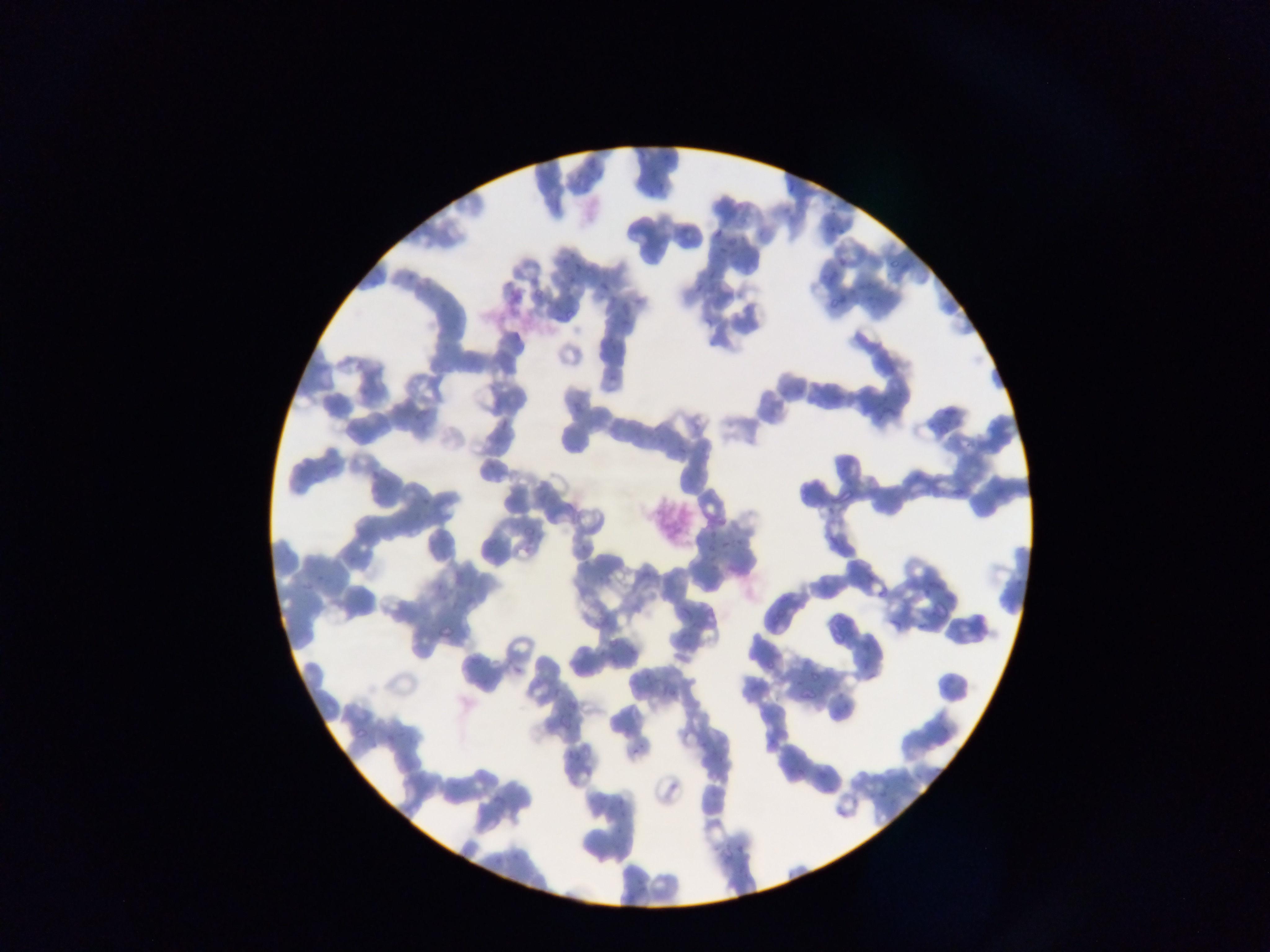

Approximate bounding boxes as (left, top, right, bottom) in pixels. Malaria parasite locations (subset; some below the resolvable size): (780, 177, 796, 195), (645, 179, 671, 194), (775, 198, 797, 224), (831, 220, 845, 233), (676, 222, 689, 236), (712, 222, 726, 236), (715, 244, 729, 258), (556, 249, 578, 267), (880, 259, 896, 277), (572, 261, 591, 274), (821, 267, 839, 287), (690, 277, 706, 299), (599, 278, 611, 290), (859, 280, 877, 303), (827, 288, 845, 310), (550, 291, 568, 313), (618, 296, 629, 317), (829, 382, 848, 401), (873, 397, 899, 422), (936, 404, 962, 424), (494, 417, 513, 437), (363, 470, 381, 488), (950, 477, 969, 496), (833, 485, 854, 504), (413, 498, 430, 509), (705, 518, 720, 548), (724, 525, 750, 550), (509, 542, 542, 559), (297, 580, 317, 596), (440, 620, 455, 642), (510, 658, 529, 682), (561, 694, 579, 723), (346, 720, 379, 747), (629, 746, 635, 755), (788, 762, 806, 780), (869, 775, 899, 799), (615, 793, 629, 816), (734, 840, 746, 858). One field of view. Thin blood film. Collected in Ghana. Mobile-phone photograph taken through the microscope. Image is 1270×952 pixels.